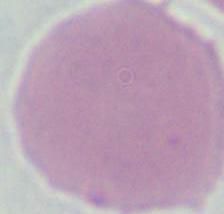
{
  "modality": "micrograph",
  "magnification": "1000x",
  "identification": "erythrocyte"
}